Classify this cell by malaria status.
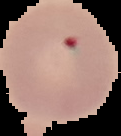

It is uninfected.

Image is 121×136 pixels. Cell region segmented out of the field of view; the surrounding area is masked to black. From a thin blood film.